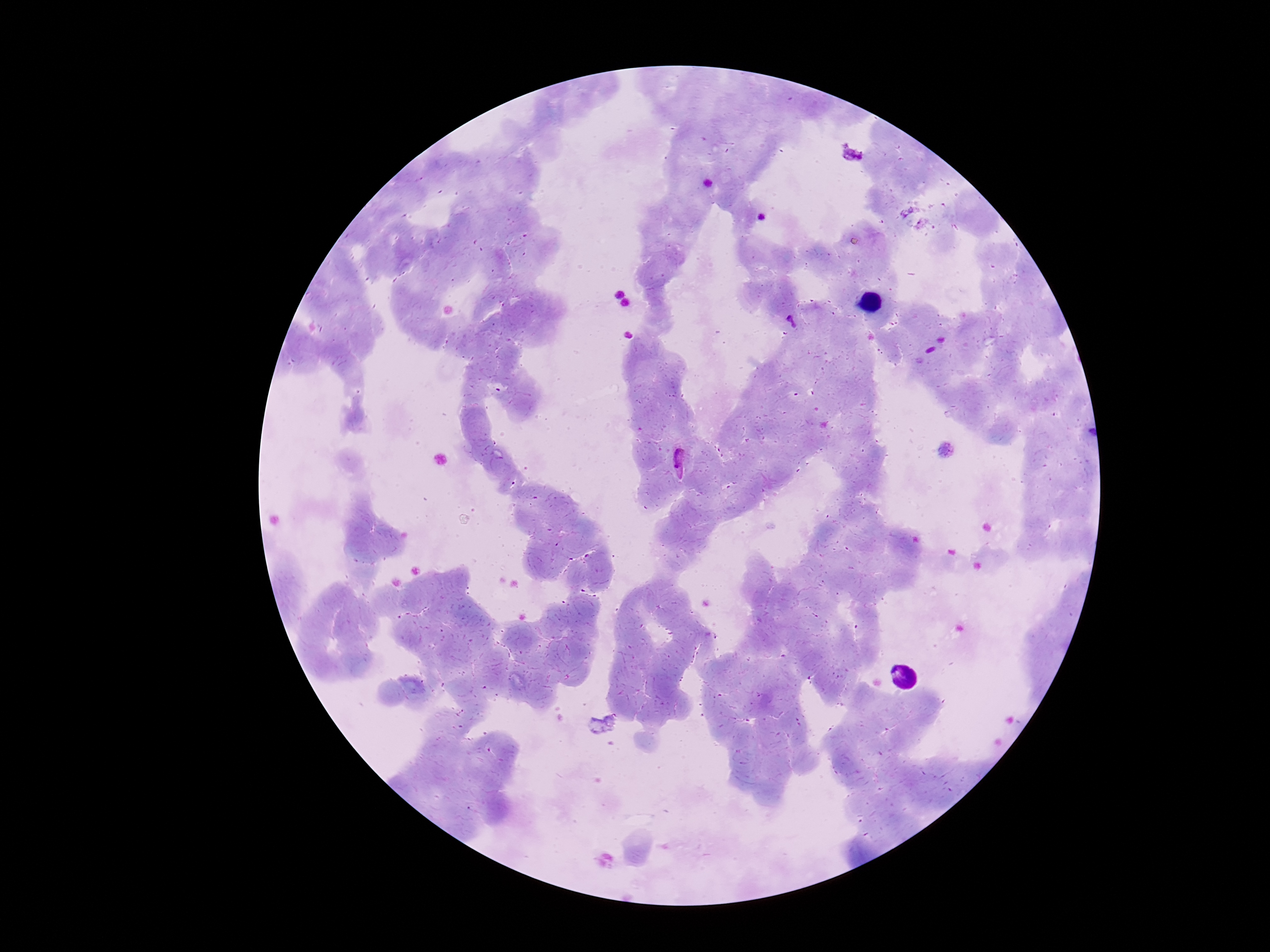 Approximate centers as [x, y] in pixels. Plasmodium parasite locations: [791, 322], [680, 465]. Photographed through the microscope eyepiece with a smartphone camera. Image is 1270×952 pixels. 100x magnification. Thick blood smear. Patient malaria status: infected. Giemsa-stained preparation. One field from this slide.